Assess this cell for malaria.
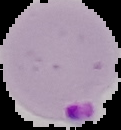

It is parasitized.

{
  "image_type": "cell region segmented out of the field of view; surrounding area masked to black",
  "preparation": "thin blood film",
  "image_size": "121×130 pixels"
}